Report the malaria status of this cell.
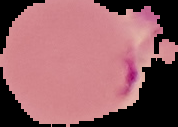

Parasitized.

preparation: thin blood film
image_type: segmented cell region on a black background
image_size: 178×127 pixels